Give the position of every malaria parasite.
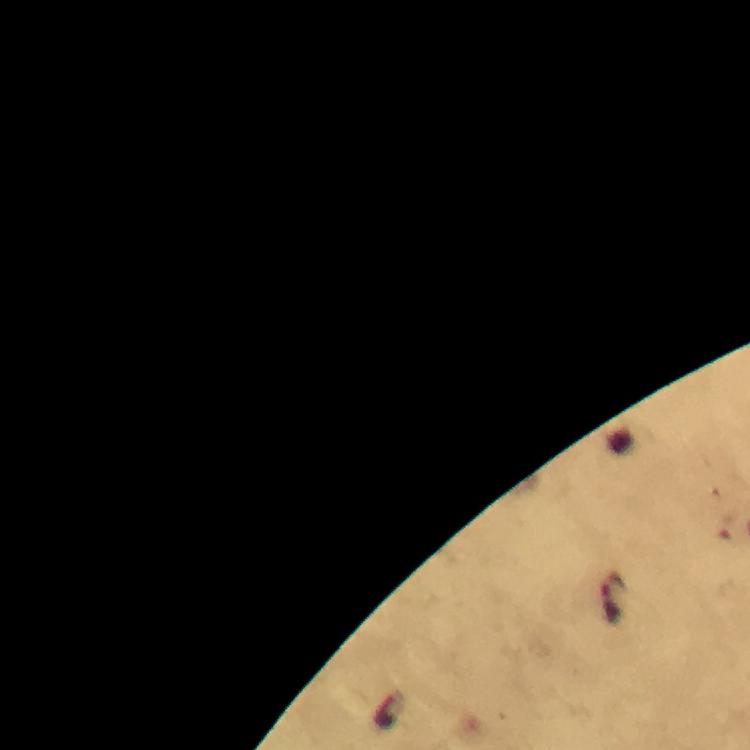

Approximate centers as [x, y] in pixels.
Malaria parasites: [614, 598].

At 100x magnification. Immersion oil was used. From a diagnostic examination for malaria. Photographed with a smartphone mounted on the microscope. Cropped region of a single field of view. Image is 750×750 pixels. Thick smear. Giemsa-stained preparation.